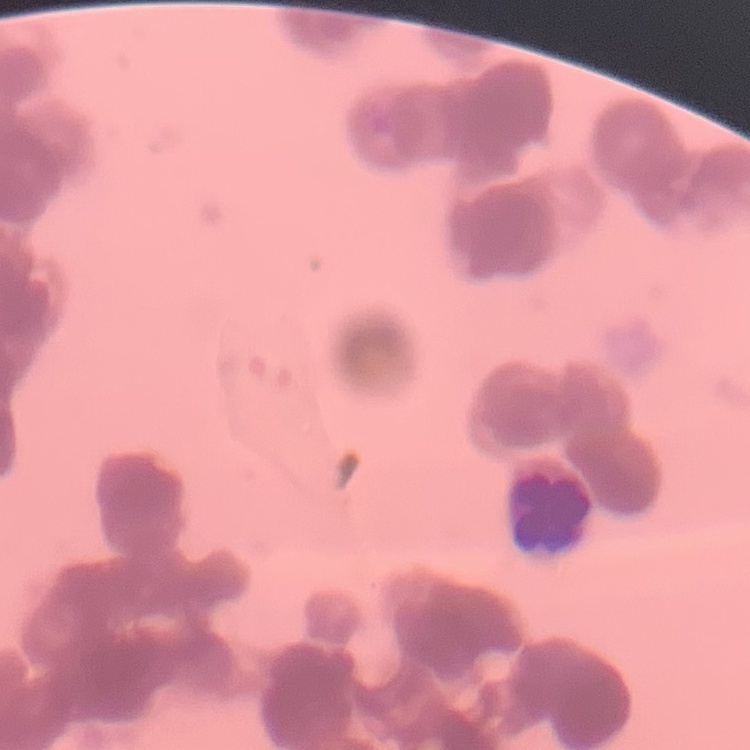
erythrocyte morphology = rouleaux formation
stain = Field's or Giemsa
preparation = thin blood smear
image type = one tile cut from a larger photomicrograph